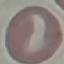
malaria status = uninfected
stain = Giemsa
image type = automatically extracted cell patch, resized to 64 × 64 pixels
capture = smartphone through the microscope eyepiece
preparation = thin smear